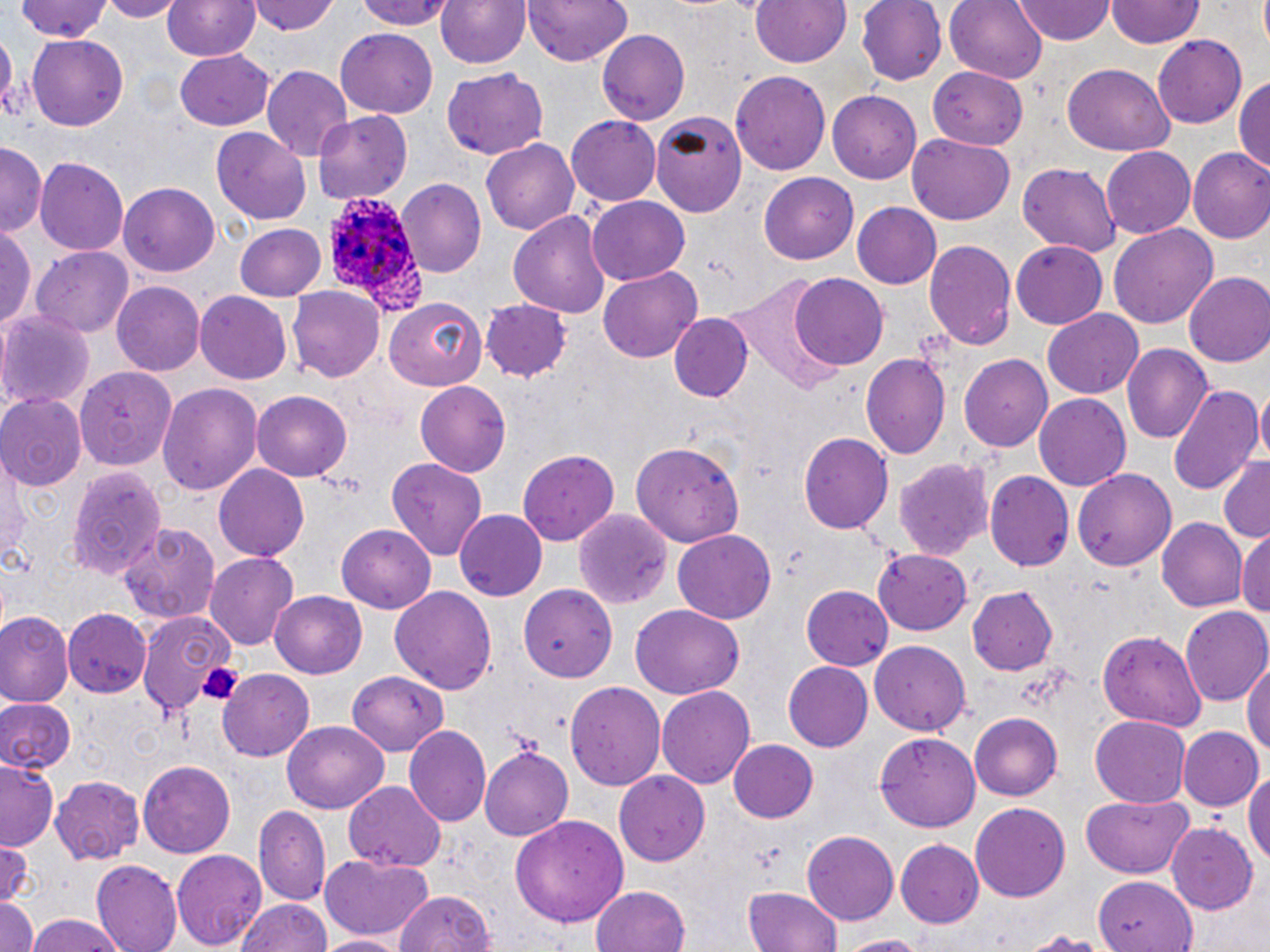 Approximate bounding boxes as named x1/y1/x2/y2 corners in pixels. Uninfected red blood cell locations: (x1=96, y1=0, x2=183, y2=21), (x1=163, y1=0, x2=259, y2=63), (x1=250, y1=0, x2=341, y2=36), (x1=357, y1=0, x2=453, y2=29), (x1=436, y1=0, x2=531, y2=71), (x1=525, y1=0, x2=634, y2=67), (x1=750, y1=0, x2=852, y2=70), (x1=856, y1=0, x2=944, y2=86), (x1=946, y1=0, x2=1048, y2=83), (x1=1016, y1=0, x2=1115, y2=44), (x1=1108, y1=0, x2=1202, y2=50), (x1=11, y1=1, x2=116, y2=43), (x1=0, y1=22, x2=15, y2=123), (x1=597, y1=29, x2=690, y2=125), (x1=336, y1=30, x2=437, y2=120), (x1=27, y1=35, x2=129, y2=130), (x1=1152, y1=35, x2=1247, y2=129), (x1=172, y1=48, x2=276, y2=131), (x1=1060, y1=63, x2=1176, y2=156), (x1=262, y1=65, x2=351, y2=160), (x1=443, y1=69, x2=549, y2=160), (x1=928, y1=69, x2=1030, y2=151), (x1=732, y1=70, x2=831, y2=176), (x1=1234, y1=72, x2=1270, y2=177), (x1=828, y1=91, x2=922, y2=181), (x1=650, y1=107, x2=750, y2=214), (x1=312, y1=110, x2=413, y2=205), (x1=566, y1=116, x2=660, y2=206), (x1=209, y1=127, x2=310, y2=224), (x1=905, y1=134, x2=1016, y2=225), (x1=481, y1=137, x2=580, y2=236), (x1=0, y1=142, x2=44, y2=239), (x1=1101, y1=147, x2=1195, y2=239), (x1=1187, y1=149, x2=1270, y2=245), (x1=35, y1=156, x2=129, y2=256), (x1=1017, y1=163, x2=1121, y2=256), (x1=758, y1=172, x2=859, y2=264), (x1=395, y1=179, x2=487, y2=279), (x1=120, y1=183, x2=220, y2=276), (x1=587, y1=197, x2=691, y2=284), (x1=851, y1=203, x2=941, y2=289), (x1=509, y1=208, x2=611, y2=322), (x1=233, y1=223, x2=326, y2=300), (x1=1110, y1=224, x2=1218, y2=329), (x1=1, y1=225, x2=36, y2=330), (x1=923, y1=239, x2=1016, y2=353), (x1=1012, y1=242, x2=1108, y2=327), (x1=33, y1=246, x2=135, y2=337), (x1=600, y1=267, x2=703, y2=363), (x1=790, y1=272, x2=888, y2=370), (x1=1184, y1=272, x2=1270, y2=366), (x1=112, y1=283, x2=207, y2=376), (x1=287, y1=287, x2=385, y2=383), (x1=195, y1=293, x2=292, y2=385), (x1=385, y1=297, x2=489, y2=389), (x1=482, y1=300, x2=573, y2=381), (x1=1043, y1=310, x2=1143, y2=399), (x1=0, y1=311, x2=93, y2=412), (x1=669, y1=314, x2=752, y2=403), (x1=1121, y1=343, x2=1213, y2=445), (x1=961, y1=353, x2=1052, y2=451), (x1=862, y1=354, x2=951, y2=459), (x1=76, y1=366, x2=178, y2=469), (x1=158, y1=382, x2=261, y2=498), (x1=415, y1=382, x2=511, y2=476), (x1=1167, y1=383, x2=1263, y2=499), (x1=1255, y1=387, x2=1270, y2=468), (x1=251, y1=391, x2=352, y2=480), (x1=0, y1=394, x2=85, y2=492), (x1=1035, y1=394, x2=1131, y2=492), (x1=799, y1=433, x2=892, y2=533), (x1=631, y1=436, x2=747, y2=544), (x1=516, y1=448, x2=620, y2=548), (x1=895, y1=456, x2=994, y2=562), (x1=1215, y1=456, x2=1270, y2=543), (x1=0, y1=458, x2=30, y2=562), (x1=388, y1=459, x2=489, y2=561), (x1=68, y1=463, x2=168, y2=577), (x1=214, y1=465, x2=309, y2=561), (x1=1072, y1=467, x2=1178, y2=569), (x1=984, y1=471, x2=1073, y2=572), (x1=453, y1=509, x2=546, y2=601), (x1=575, y1=511, x2=672, y2=609), (x1=1156, y1=518, x2=1246, y2=613), (x1=119, y1=520, x2=221, y2=624), (x1=336, y1=523, x2=435, y2=613), (x1=1238, y1=529, x2=1270, y2=624), (x1=673, y1=530, x2=776, y2=624), (x1=872, y1=548, x2=974, y2=634), (x1=205, y1=552, x2=298, y2=652), (x1=518, y1=583, x2=614, y2=679), (x1=802, y1=584, x2=894, y2=669), (x1=966, y1=586, x2=1060, y2=676), (x1=390, y1=587, x2=499, y2=694), (x1=270, y1=589, x2=367, y2=679), (x1=1179, y1=604, x2=1269, y2=707), (x1=631, y1=606, x2=742, y2=697), (x1=64, y1=608, x2=148, y2=698), (x1=1, y1=611, x2=70, y2=706), (x1=139, y1=612, x2=236, y2=717), (x1=1097, y1=630, x2=1207, y2=732), (x1=868, y1=640, x2=971, y2=737), (x1=1243, y1=653, x2=1270, y2=767), (x1=785, y1=661, x2=875, y2=752), (x1=345, y1=669, x2=451, y2=752), (x1=217, y1=670, x2=315, y2=761), (x1=567, y1=681, x2=667, y2=791), (x1=658, y1=685, x2=755, y2=792), (x1=0, y1=695, x2=75, y2=776), (x1=969, y1=713, x2=1062, y2=800), (x1=1088, y1=715, x2=1192, y2=808), (x1=284, y1=721, x2=390, y2=812), (x1=406, y1=725, x2=490, y2=827), (x1=1175, y1=725, x2=1263, y2=812), (x1=875, y1=730, x2=980, y2=833), (x1=728, y1=738, x2=817, y2=823), (x1=480, y1=746, x2=574, y2=839), (x1=0, y1=759, x2=61, y2=847), (x1=137, y1=760, x2=236, y2=856), (x1=1244, y1=766, x2=1270, y2=874), (x1=614, y1=770, x2=709, y2=867), (x1=51, y1=775, x2=146, y2=865), (x1=344, y1=781, x2=447, y2=872), (x1=1080, y1=794, x2=1195, y2=879), (x1=968, y1=802, x2=1071, y2=903), (x1=254, y1=806, x2=331, y2=906), (x1=508, y1=812, x2=630, y2=929), (x1=1167, y1=823, x2=1259, y2=916), (x1=801, y1=831, x2=898, y2=926), (x1=895, y1=838, x2=985, y2=927), (x1=0, y1=841, x2=34, y2=907), (x1=173, y1=849, x2=267, y2=952), (x1=318, y1=853, x2=436, y2=943), (x1=89, y1=860, x2=183, y2=952), (x1=1094, y1=878, x2=1199, y2=952), (x1=741, y1=885, x2=845, y2=952), (x1=591, y1=886, x2=691, y2=952), (x1=394, y1=889, x2=497, y2=952), (x1=235, y1=896, x2=332, y2=952), (x1=0, y1=898, x2=39, y2=952), (x1=22, y1=915, x2=129, y2=952), (x1=1015, y1=929, x2=1122, y2=951), (x1=317, y1=932, x2=403, y2=951), (x1=835, y1=935, x2=932, y2=952). Platelet locations: (x1=196, y1=658, x2=245, y2=705). Plasmodium ovale-infected red blood cell locations: (x1=320, y1=192, x2=427, y2=315). Slide-level diagnosis: Plasmodium ovale. Thin blood smear. One field of a larger specimen. Light microscopy. Captured at 1000x magnification. May-Grünwald-Giemsa stain. Image is 1270×952 pixels.